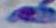

1000x magnification. Photomicrograph. Toxoplasma gondii is shown.